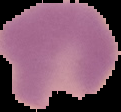

Image is 121×112 pixels. Result: malaria parasites detected. From a thin blood film. Segmented cell region on a black background.